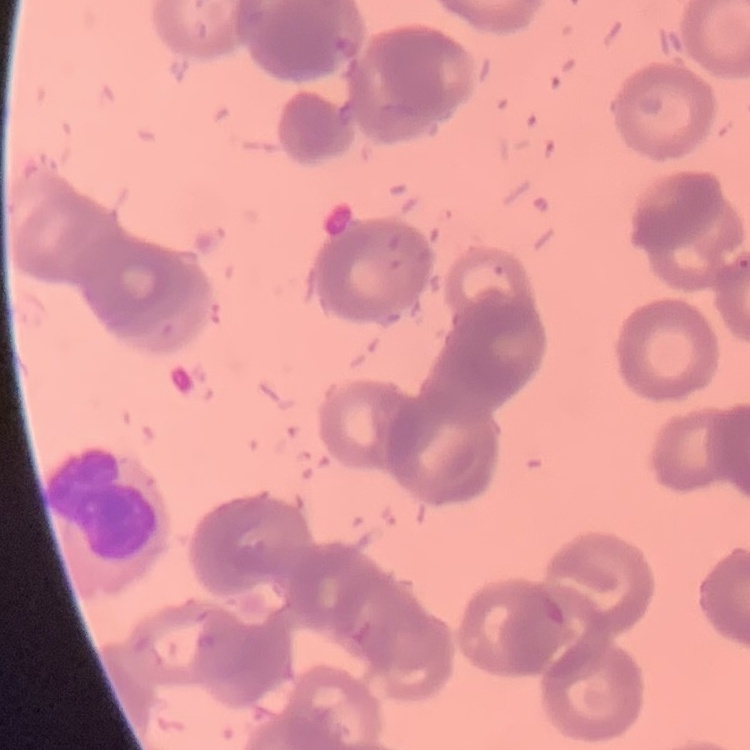
Summary:
  - Red blood cell morphology: rouleaux formation
  - Stain: Field's or Giemsa
  - Image type: one tile cut from a larger photomicrograph
  - Preparation: thin blood smear